Comment on the morphology of the red blood cells.
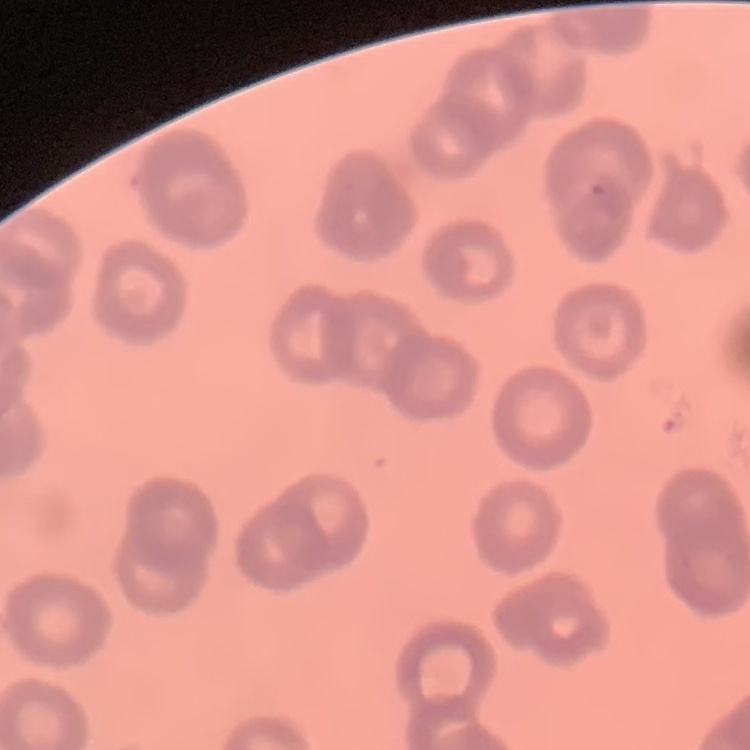

Rouleaux formation.

Square crop of a larger photomicrograph. Thin blood smear. Stained with either Field's or Giemsa.